Comment on the morphology of the red blood cells.
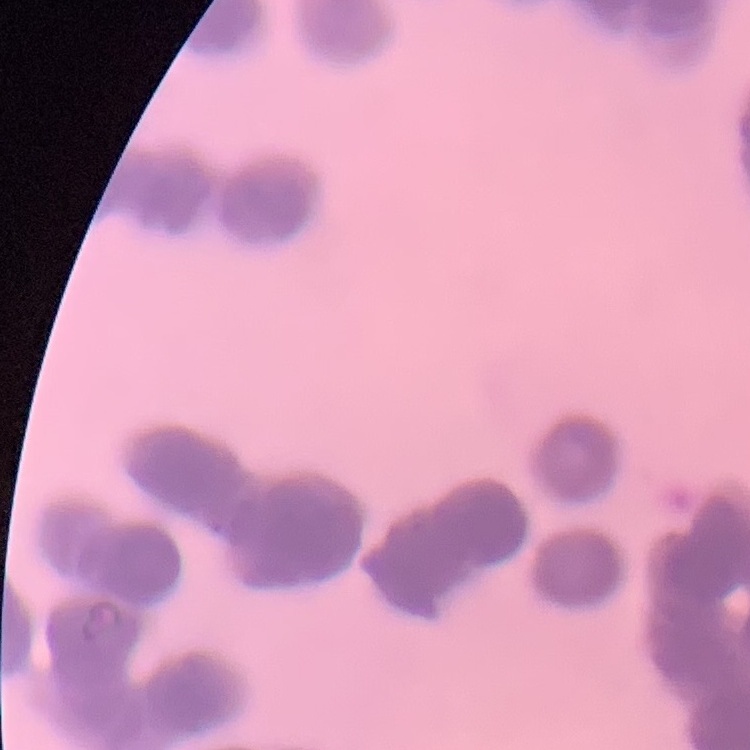

They show rouleaux formation.

preparation: thin peripheral smear
stain: Field's or Giemsa
image_type: square crop of a larger photomicrograph